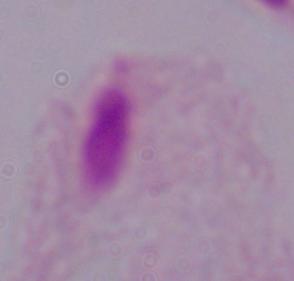
{
  "magnification": "1000x",
  "identification": "trichomonad",
  "modality": "photomicrograph"
}